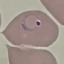
Result: malaria parasites identified. Thin smear of blood. Cell patch, automatically extracted from a larger field of view and resized to 64 × 64 pixels. Acquired by smartphone through the microscope eyepiece. Giemsa-stained preparation.